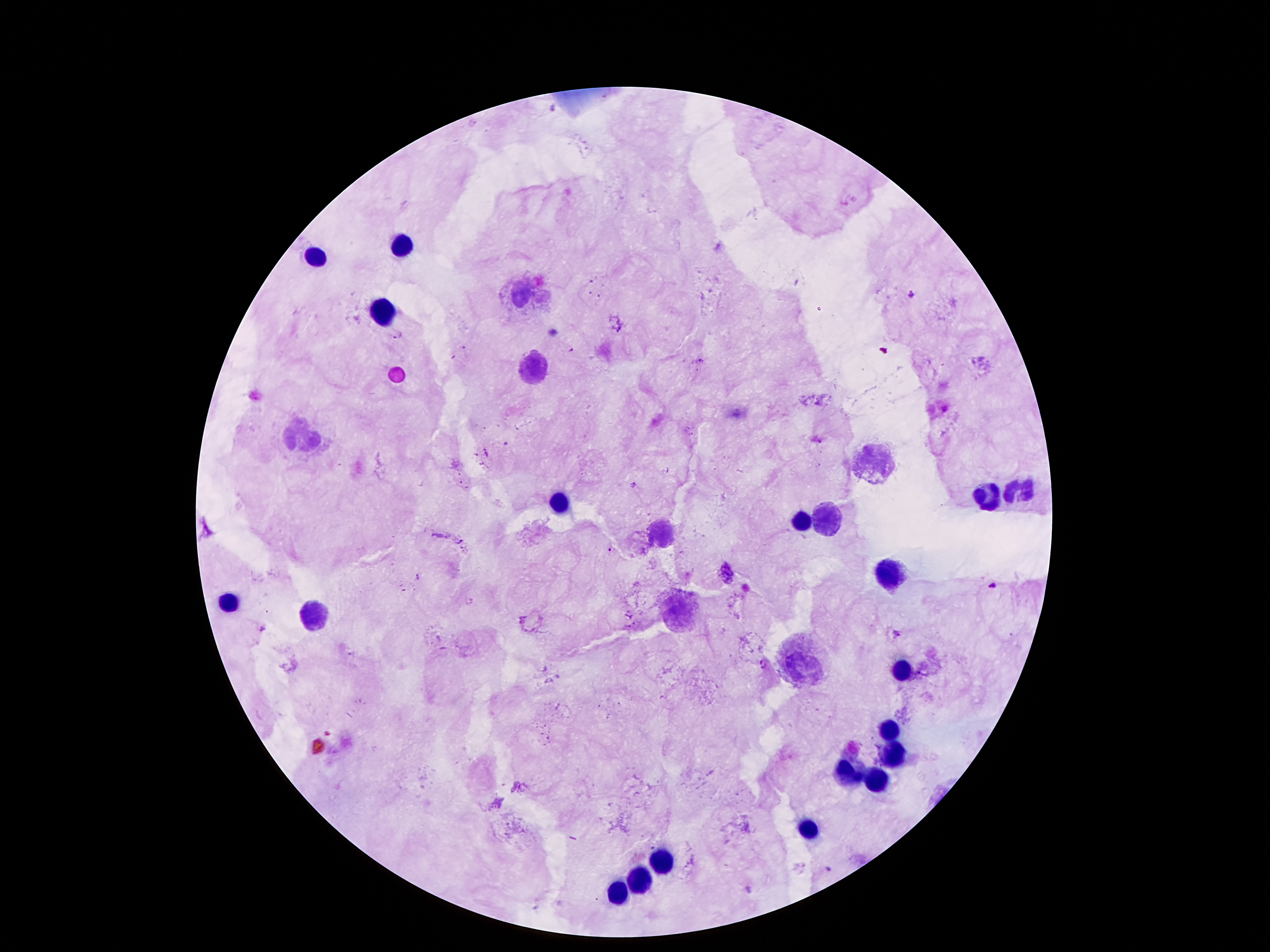

coordinate format = approximate centers as (x, y) in pixels
leukocyte locations = (398, 246), (317, 257), (523, 296), (382, 313), (537, 368), (301, 436), (871, 463), (1018, 492), (988, 497), (559, 502), (796, 520), (821, 520), (659, 531), (893, 572), (232, 601), (679, 610), (314, 615), (805, 665), (902, 669), (888, 729), (895, 754), (845, 772), (877, 778), (807, 828), (659, 860), (645, 881), (620, 895)
malaria parasite locations = (912, 295), (395, 333), (572, 350), (486, 452), (632, 485), (609, 548), (417, 576), (991, 585), (523, 620), (261, 628), (896, 632), (761, 665), (826, 868)
stain = Giemsa
image size = 1270×952 pixels
patient malaria status = positive for Plasmodium falciparum
capture = smartphone through the microscope eyepiece
field of view = one from this slide
magnification = 100x
preparation = thick blood film